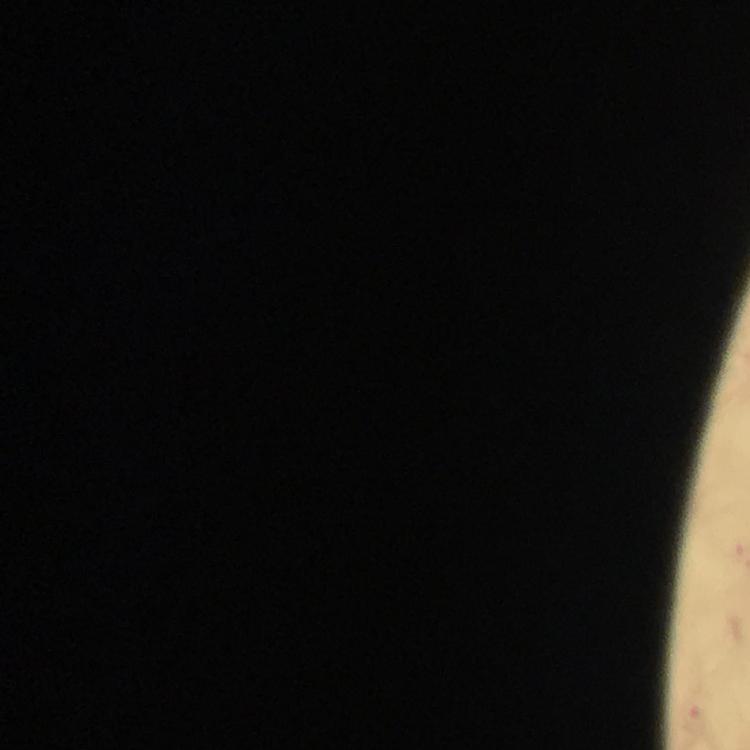 Approximate object centers, in pixels from the top-left corner. Malaria parasite locations: (x=694, y=719). At 100x magnification. Thick blood smear. From a malaria diagnostic workup. Image is 750×750 pixels. Smartphone photograph taken through a microscope. Giemsa-stained preparation. Cropped region of a single field of view. Immersion oil applied.